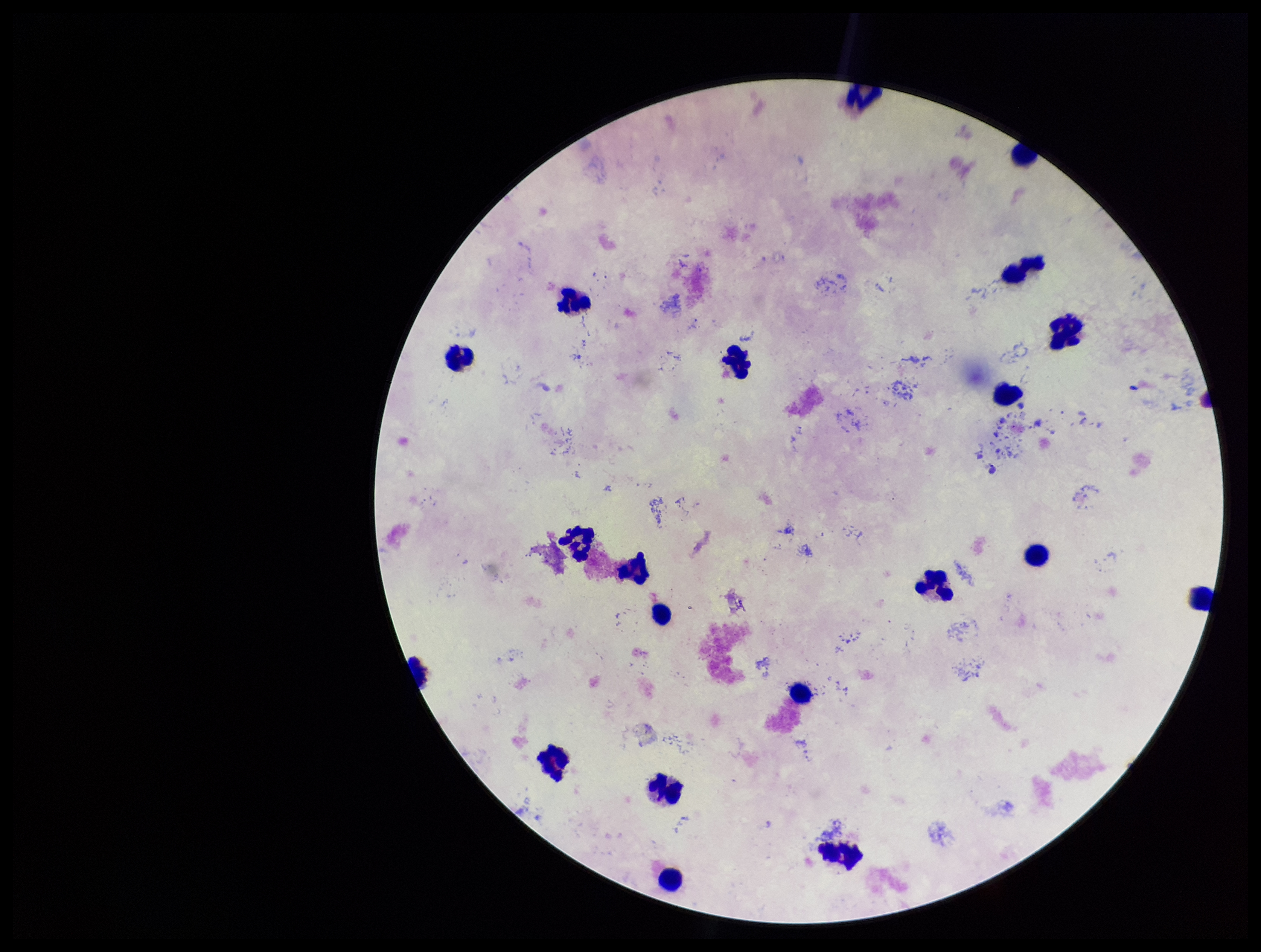 Image is 1261×952 pixels. Photographed through the microscope eyepiece with a smartphone camera. Patient malaria status: negative. Preparation: thick smear. Plasmodium parasites: none seen. Leukocyte count: 20. One field from this slide. Giemsa stain. Parasite count: 0.